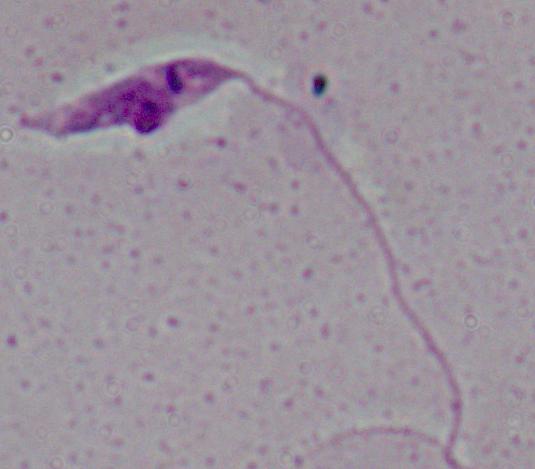
{
  "identification": "Leishmania",
  "magnification": "1000x",
  "modality": "micrograph"
}